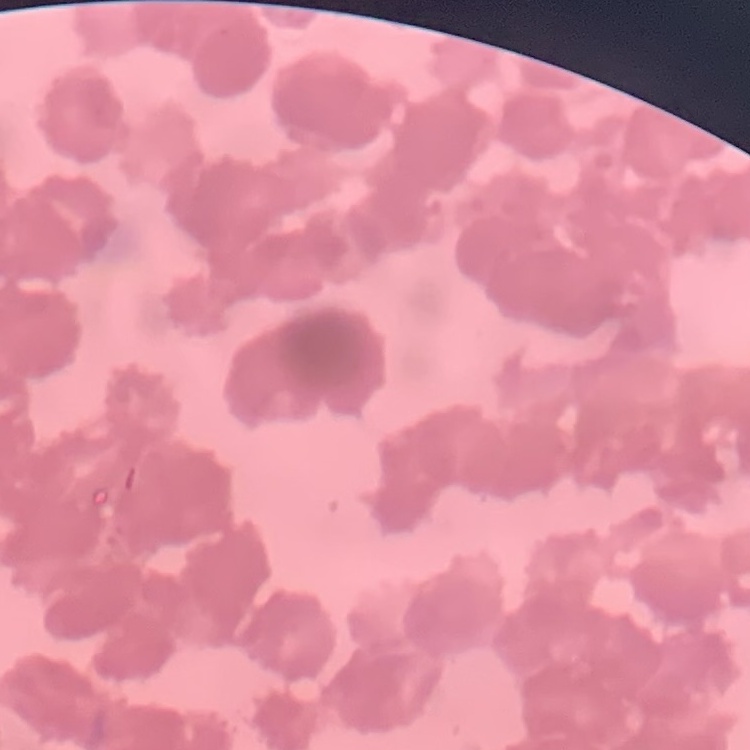

Summary:
  - Erythrocyte morphology: rouleaux formation
  - Stain: Field's or Giemsa
  - Preparation: thin peripheral smear
  - Image type: square crop of a larger photomicrograph